Identify the parasite.
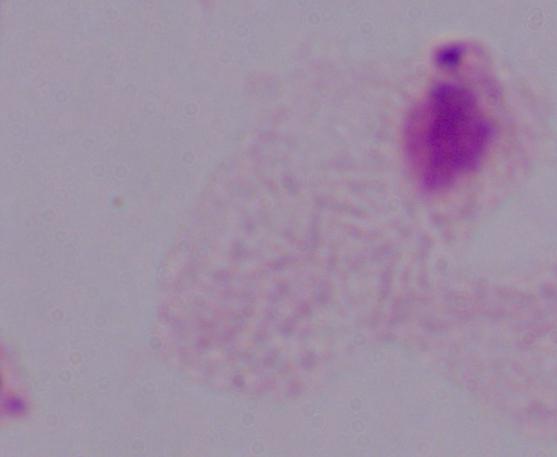
A trichomonad.

Summary:
  - Modality: micrograph
  - Magnification: 1000x